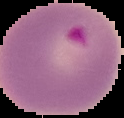
preparation: thin blood film
malaria_status: parasitized
image_size: 124×118 pixels
image_type: cell region segmented out of the field of view; surrounding area masked to black